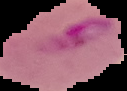

Summary:
  - Image type: segmented cell region on a black background
  - Preparation: thin blood smear
  - Malaria status: parasitized
  - Image size: 127×91 pixels